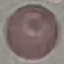 Result: no malaria parasites seen. Cell patch, automatically extracted from a larger field of view and resized to 64 × 64 pixels. Giemsa-stained preparation. Thin blood film. Photographed with a smartphone camera at the microscope eyepiece.